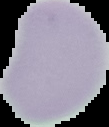

result = negative for malaria parasites
image size = 109×127 pixels
image type = cell region segmented out of the field of view; surrounding area masked to black
preparation = thin blood film